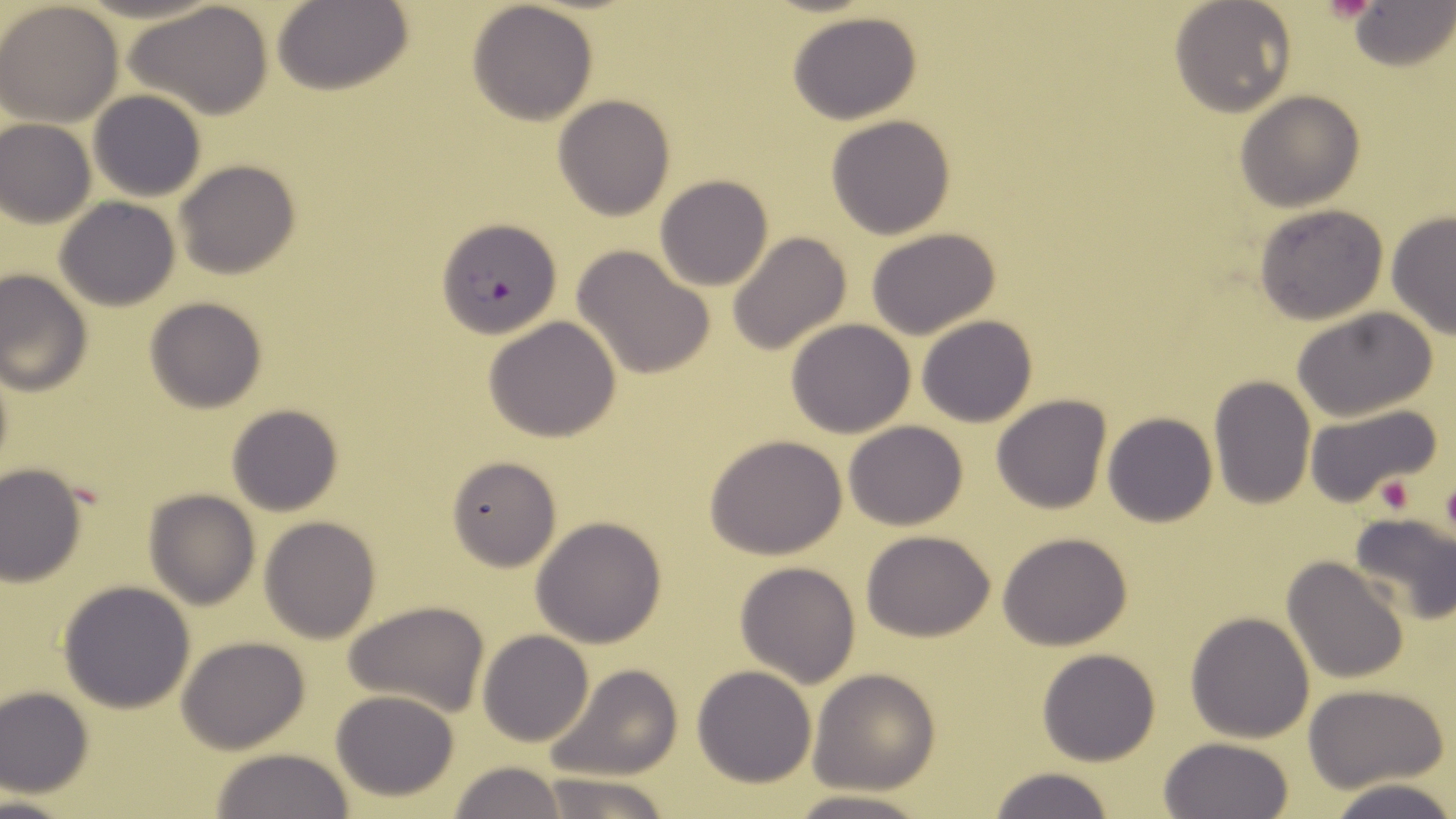

Summary:
  - Coordinate format: approximate bounding boxes as [x1, y1, x2, y2] in pixels
  - Platelet locations: [1440, 474, 1456, 544], [1374, 475, 1416, 514]
  - Uninfected red blood cell locations: [1169, 0, 1297, 116], [128, 1, 274, 118], [274, 1, 412, 96], [466, 1, 599, 124], [1347, 1, 1454, 71], [0, 2, 124, 127], [788, 11, 923, 125], [1234, 89, 1365, 212], [89, 90, 207, 202], [552, 94, 676, 221], [826, 115, 957, 240], [0, 119, 95, 227], [174, 160, 301, 281], [654, 175, 774, 291], [55, 196, 181, 311], [1252, 204, 1389, 325], [1386, 211, 1456, 341], [864, 227, 1002, 341], [727, 233, 853, 357], [572, 246, 714, 379], [0, 269, 92, 395], [144, 296, 268, 414], [1291, 308, 1437, 420], [917, 314, 1037, 427], [483, 315, 624, 442], [786, 318, 917, 438], [1209, 378, 1316, 508], [991, 394, 1111, 514], [1304, 402, 1445, 511], [226, 403, 342, 515], [1103, 412, 1217, 527], [843, 421, 968, 531], [704, 433, 848, 558], [446, 454, 562, 571], [0, 463, 87, 585], [143, 489, 262, 609], [1348, 511, 1456, 624], [259, 516, 381, 643], [532, 516, 666, 647], [862, 531, 995, 641], [997, 531, 1135, 650], [1282, 556, 1408, 685], [734, 561, 861, 687], [58, 581, 196, 713], [344, 600, 491, 716], [1186, 610, 1315, 743], [479, 630, 593, 746], [176, 637, 311, 753], [1036, 647, 1162, 766], [543, 664, 684, 783], [692, 665, 816, 787], [809, 669, 942, 793], [1302, 683, 1450, 793], [0, 686, 95, 797], [330, 689, 462, 802], [1160, 737, 1294, 819], [209, 746, 354, 819], [448, 761, 566, 818], [988, 767, 1114, 819], [534, 773, 674, 819], [1322, 778, 1456, 819], [784, 791, 934, 819]
  - Plasmodium falciparum-infected red blood cell locations: [436, 217, 562, 339]
  - Slide-level diagnosis: Plasmodium falciparum
  - Preparation: thin blood smear
  - Stain: May-Grünwald-Giemsa
  - Magnification: 1000x
  - Field of view: single
  - Image size: 1456×819 pixels
  - Modality: light microscopy